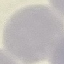
Summary:
  - Malaria status: uninfected
  - Capture: smartphone camera at the microscope eyepiece
  - Image type: automatically extracted cell patch, resized to 64 × 64 pixels
  - Stain: Giemsa
  - Preparation: thin blood film